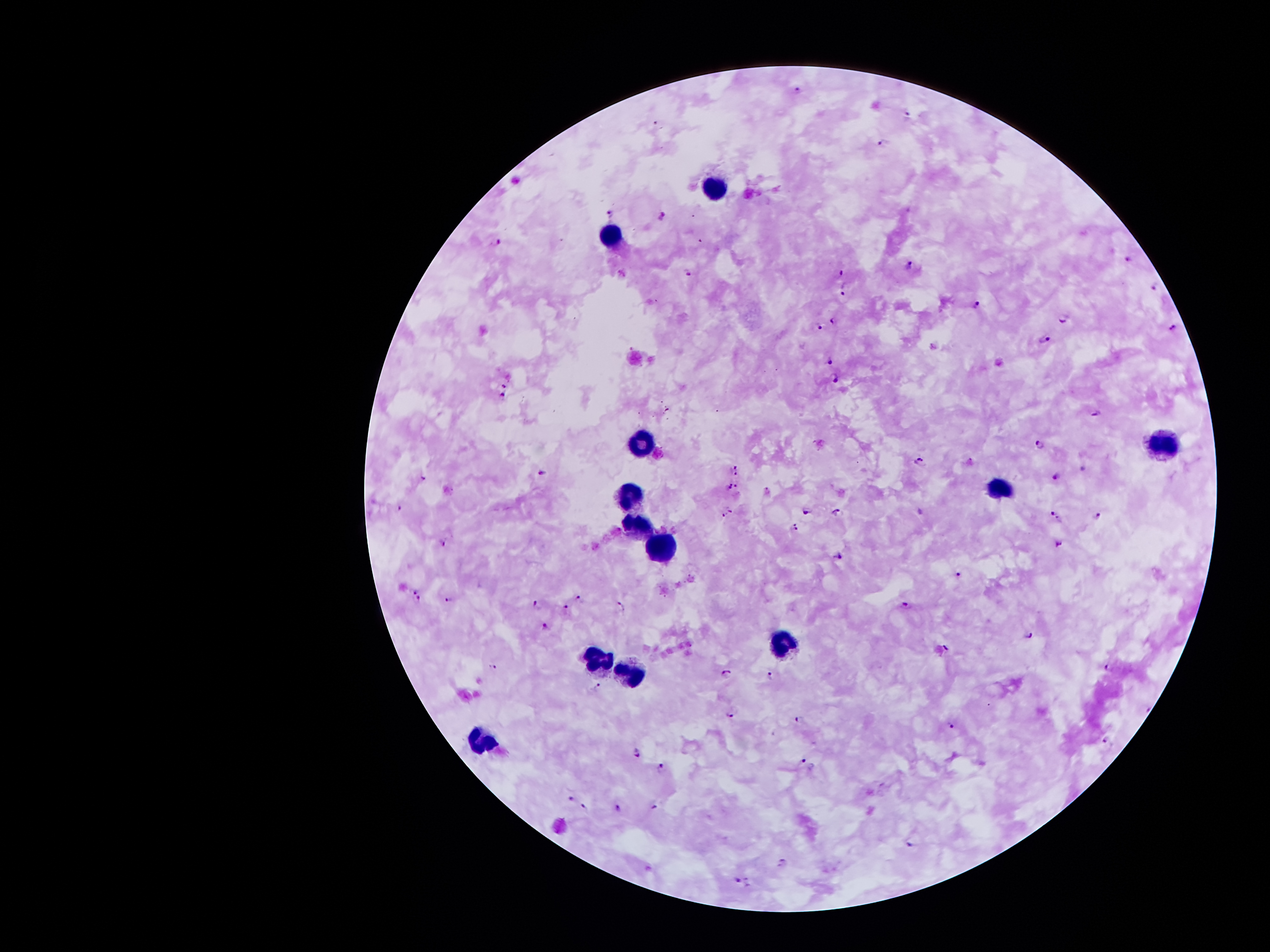

Approximate centers as [x, y] in pixels.
Summary:
  - Plasmodium parasite locations: [798, 92], [909, 116], [658, 124], [882, 145], [608, 211], [662, 218], [499, 240], [1129, 259], [910, 264], [687, 272], [842, 273], [844, 290], [1155, 290], [977, 302], [835, 321], [1065, 321], [819, 326], [1172, 327], [1046, 339], [830, 360], [835, 378], [504, 385], [501, 398], [1098, 412], [1040, 445], [922, 461], [1083, 468], [737, 470], [543, 474], [1057, 475], [423, 478], [738, 485], [729, 486], [400, 508], [807, 510], [730, 511], [838, 512], [724, 516], [1055, 517], [1097, 517], [796, 526], [444, 541], [1060, 541], [838, 556], [962, 575], [416, 588], [449, 600], [581, 600], [418, 601], [908, 605], [538, 607], [566, 609], [619, 609], [545, 628], [1028, 633], [948, 645], [1110, 666], [496, 669], [727, 673], [771, 675], [597, 687], [734, 712], [800, 721], [952, 725], [1108, 740], [638, 754], [803, 760], [661, 769], [571, 801], [585, 807], [655, 807], [617, 809], [913, 840], [783, 863], [735, 880], [750, 882]
  - Leukocyte locations: [714, 182], [609, 240], [643, 441], [1169, 441], [1005, 489], [629, 496], [634, 523], [660, 543], [782, 645], [593, 657], [630, 676], [486, 741]
  - Stain: Giemsa
  - Patient malaria status: positive for Plasmodium falciparum
  - Preparation: thick peripheral-blood smear
  - Magnification: 100x
  - Field of view: one from this slide
  - Image size: 1270×952 pixels
  - Capture: smartphone through the microscope eyepiece